Name the blood parasite species.
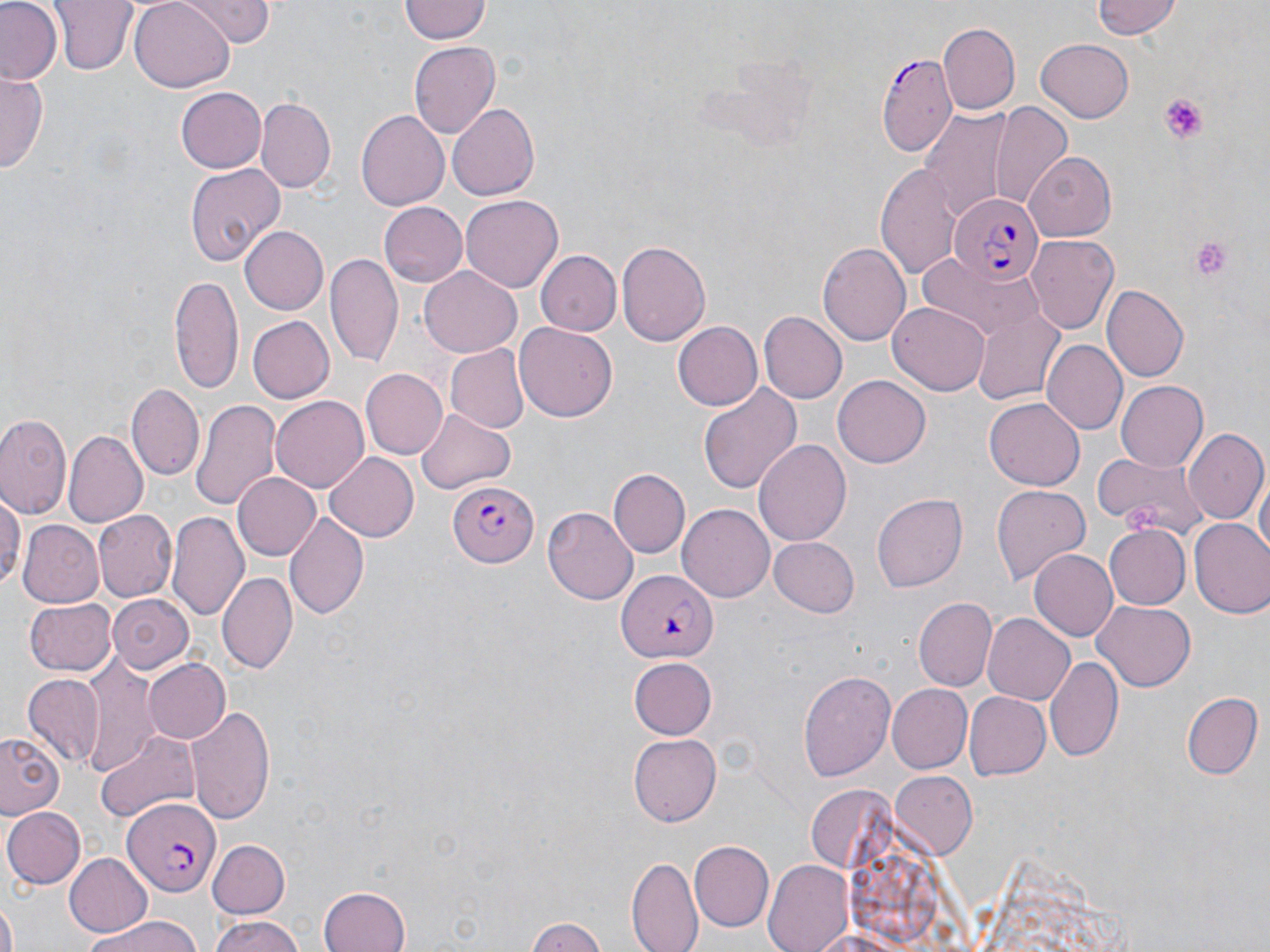

Plasmodium falciparum.

{
  "modality": "light microscopy",
  "stain": "May-Grünwald-Giemsa",
  "platelet_locations": "approximate bounding boxes as named x1/y1/x2/y2 corners in pixels: (x1=1159, y1=94, x2=1209, y2=146), (x1=1188, y1=237, x2=1235, y2=284), (x1=1124, y1=502, x2=1165, y2=538)",
  "field_of_view": "one of a larger specimen",
  "plasmodium_falciparum_infected_red_blood_cell_locations": "approximate bounding boxes as named x1/y1/x2/y2 corners in pixels: (x1=877, y1=52, x2=957, y2=159), (x1=949, y1=195, x2=1040, y2=284), (x1=447, y1=483, x2=540, y2=566), (x1=618, y1=568, x2=716, y2=663), (x1=122, y1=797, x2=218, y2=897)",
  "uninfected_red_blood_cell_locations": "approximate bounding boxes as named x1/y1/x2/y2 corners in pixels: (x1=0, y1=0, x2=64, y2=84), (x1=51, y1=0, x2=134, y2=75), (x1=130, y1=0, x2=232, y2=88), (x1=181, y1=0, x2=273, y2=45), (x1=401, y1=0, x2=490, y2=44), (x1=1088, y1=0, x2=1183, y2=40), (x1=938, y1=22, x2=1021, y2=114), (x1=1035, y1=39, x2=1135, y2=123), (x1=408, y1=41, x2=499, y2=140), (x1=0, y1=72, x2=46, y2=175), (x1=176, y1=86, x2=267, y2=173), (x1=254, y1=98, x2=335, y2=193), (x1=448, y1=102, x2=541, y2=202), (x1=993, y1=104, x2=1074, y2=202), (x1=917, y1=105, x2=1034, y2=219), (x1=356, y1=109, x2=450, y2=210), (x1=1022, y1=152, x2=1117, y2=240), (x1=185, y1=162, x2=285, y2=268), (x1=876, y1=163, x2=961, y2=279), (x1=461, y1=195, x2=564, y2=291), (x1=376, y1=201, x2=467, y2=288), (x1=241, y1=226, x2=328, y2=314), (x1=1027, y1=234, x2=1119, y2=335), (x1=616, y1=239, x2=711, y2=347), (x1=818, y1=240, x2=912, y2=349), (x1=325, y1=251, x2=402, y2=366), (x1=538, y1=251, x2=621, y2=334), (x1=920, y1=253, x2=1044, y2=339), (x1=419, y1=266, x2=522, y2=356), (x1=169, y1=272, x2=244, y2=393), (x1=1104, y1=285, x2=1187, y2=381), (x1=889, y1=304, x2=990, y2=394), (x1=971, y1=309, x2=1067, y2=407), (x1=758, y1=311, x2=846, y2=404), (x1=246, y1=315, x2=335, y2=404), (x1=514, y1=322, x2=617, y2=422), (x1=673, y1=322, x2=762, y2=410), (x1=1042, y1=340, x2=1128, y2=435), (x1=444, y1=345, x2=529, y2=433), (x1=360, y1=368, x2=447, y2=460), (x1=832, y1=376, x2=931, y2=469), (x1=697, y1=381, x2=800, y2=494), (x1=1116, y1=381, x2=1209, y2=471), (x1=127, y1=384, x2=204, y2=481), (x1=270, y1=395, x2=369, y2=492), (x1=985, y1=397, x2=1086, y2=491), (x1=192, y1=398, x2=280, y2=514), (x1=418, y1=408, x2=514, y2=492), (x1=0, y1=413, x2=70, y2=520), (x1=1185, y1=428, x2=1268, y2=524), (x1=66, y1=431, x2=146, y2=526), (x1=753, y1=437, x2=850, y2=544), (x1=325, y1=450, x2=419, y2=541), (x1=1095, y1=450, x2=1209, y2=538), (x1=609, y1=470, x2=688, y2=556), (x1=232, y1=472, x2=322, y2=562), (x1=1253, y1=473, x2=1268, y2=565), (x1=570, y1=482, x2=684, y2=580), (x1=993, y1=485, x2=1089, y2=585), (x1=0, y1=490, x2=24, y2=592), (x1=873, y1=493, x2=967, y2=592), (x1=677, y1=505, x2=775, y2=602), (x1=542, y1=507, x2=638, y2=604), (x1=93, y1=510, x2=177, y2=601), (x1=167, y1=510, x2=249, y2=619), (x1=283, y1=512, x2=369, y2=623), (x1=1189, y1=519, x2=1270, y2=619), (x1=15, y1=520, x2=103, y2=609), (x1=1103, y1=524, x2=1191, y2=610), (x1=769, y1=537, x2=860, y2=617), (x1=1028, y1=549, x2=1116, y2=643), (x1=220, y1=571, x2=296, y2=671), (x1=105, y1=593, x2=196, y2=673), (x1=914, y1=596, x2=998, y2=691), (x1=24, y1=598, x2=115, y2=676), (x1=1094, y1=601, x2=1195, y2=691), (x1=982, y1=612, x2=1076, y2=704), (x1=76, y1=655, x2=163, y2=774), (x1=1047, y1=655, x2=1123, y2=763), (x1=143, y1=658, x2=230, y2=743), (x1=630, y1=659, x2=715, y2=739), (x1=799, y1=670, x2=895, y2=784), (x1=22, y1=675, x2=103, y2=764), (x1=885, y1=683, x2=971, y2=773), (x1=963, y1=691, x2=1051, y2=782), (x1=1183, y1=692, x2=1261, y2=779), (x1=11, y1=695, x2=88, y2=794), (x1=189, y1=703, x2=277, y2=825), (x1=1, y1=732, x2=63, y2=815), (x1=96, y1=732, x2=199, y2=822), (x1=627, y1=733, x2=719, y2=826), (x1=888, y1=771, x2=976, y2=861), (x1=805, y1=785, x2=900, y2=875), (x1=1, y1=805, x2=85, y2=890), (x1=207, y1=838, x2=290, y2=915), (x1=690, y1=842, x2=773, y2=930), (x1=64, y1=852, x2=151, y2=936), (x1=628, y1=857, x2=702, y2=951), (x1=764, y1=863, x2=856, y2=952), (x1=319, y1=886, x2=411, y2=952), (x1=1, y1=902, x2=18, y2=952), (x1=79, y1=915, x2=199, y2=952), (x1=206, y1=915, x2=311, y2=952), (x1=524, y1=916, x2=610, y2=952), (x1=802, y1=927, x2=916, y2=952)",
  "image_size": "1270×952 pixels",
  "preparation": "thin blood film",
  "magnification": "1000x"
}